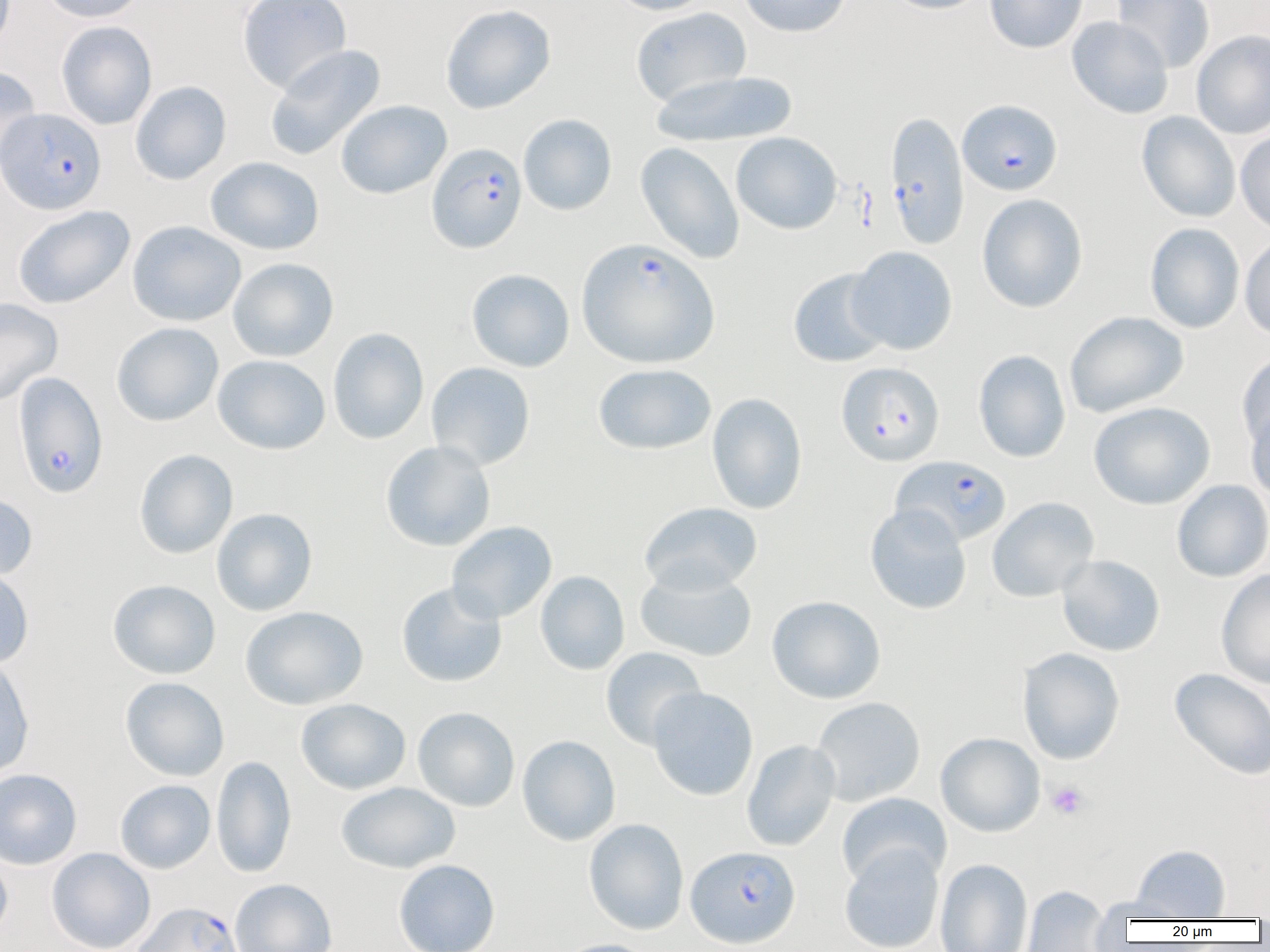

slide-level diagnosis = Plasmodium falciparum
magnification = 1000x
preparation = thin blood film
modality = light microscopy
platelet locations = approximate bounding boxes as (x1,y1)-(x2,y2) corner pairs in pixels: (1047,781)-(1090,821)
Plasmodium falciparum-infected red blood cell locations = approximate bounding boxes as (x1,y1)-(x2,y2) corner pairs in pixels: (957,99)-(1062,196), (0,108)-(106,214), (884,112)-(970,250), (427,143)-(527,253), (576,237)-(720,368), (836,362)-(945,467), (12,372)-(108,499), (891,455)-(1011,547), (685,845)-(801,948), (130,901)-(245,952)
image size = 1270×952 pixels
uninfected red blood cell locations = approximate bounding boxes as (x1,y1)-(x2,y2) corner pairs in pixels: (40,0)-(147,23), (237,0)-(351,93), (608,0)-(713,15), (738,0)-(851,37), (884,0)-(991,14), (984,0)-(1088,53), (1112,0)-(1215,72), (440,4)-(556,114), (630,7)-(752,106), (1067,16)-(1173,119), (56,21)-(157,130), (1191,29)-(1270,139), (264,44)-(386,162), (0,66)-(42,176), (650,70)-(798,148), (130,81)-(232,185), (336,99)-(452,199), (1137,111)-(1241,222), (518,114)-(617,216), (1236,128)-(1270,235), (731,132)-(842,235), (636,142)-(744,264), (205,156)-(325,255), (976,193)-(1088,313), (11,205)-(136,309), (127,221)-(246,327), (1144,223)-(1245,334), (1239,234)-(1270,341), (847,246)-(958,355), (227,258)-(339,362), (466,268)-(575,372), (788,268)-(892,368), (0,297)-(64,406), (1065,311)-(1188,418), (112,322)-(224,426), (327,327)-(429,444), (973,350)-(1071,463), (1237,352)-(1270,452), (213,354)-(331,455), (426,362)-(536,471), (593,363)-(717,455), (706,392)-(808,514), (1088,401)-(1216,510), (1245,401)-(1270,503), (380,440)-(496,552), (134,449)-(238,559), (1171,479)-(1270,583), (0,492)-(38,582), (987,496)-(1100,602), (639,502)-(763,595), (865,503)-(972,614), (211,508)-(318,616), (446,521)-(557,623), (1057,554)-(1165,656), (634,566)-(758,663), (0,567)-(34,668), (1216,569)-(1270,688), (535,570)-(630,675), (107,579)-(221,680), (396,582)-(507,688), (766,595)-(887,704), (240,606)-(368,710), (600,647)-(707,750), (1017,647)-(1125,764), (0,656)-(35,780), (1168,667)-(1270,782), (119,677)-(230,781), (647,686)-(759,801), (811,696)-(926,806), (295,698)-(411,794), (413,707)-(520,812), (936,732)-(1045,837), (517,735)-(621,846), (741,739)-(841,852), (211,755)-(297,878), (0,768)-(82,869), (115,779)-(216,874), (336,782)-(461,873), (836,792)-(951,889), (583,818)-(689,934), (839,843)-(945,952), (1132,844)-(1230,921), (46,847)-(156,952), (0,852)-(13,944), (935,858)-(1033,952), (393,859)-(501,952), (229,878)-(337,952), (1022,885)-(1111,951), (1093,896)-(1199,923), (553,938)-(659,952)
field of view = one of a larger specimen